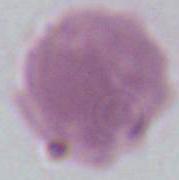

Summary:
  - Identification: red blood cell
  - Modality: micrograph
  - Magnification: 1000x